Outline each blood parasite and name the species.
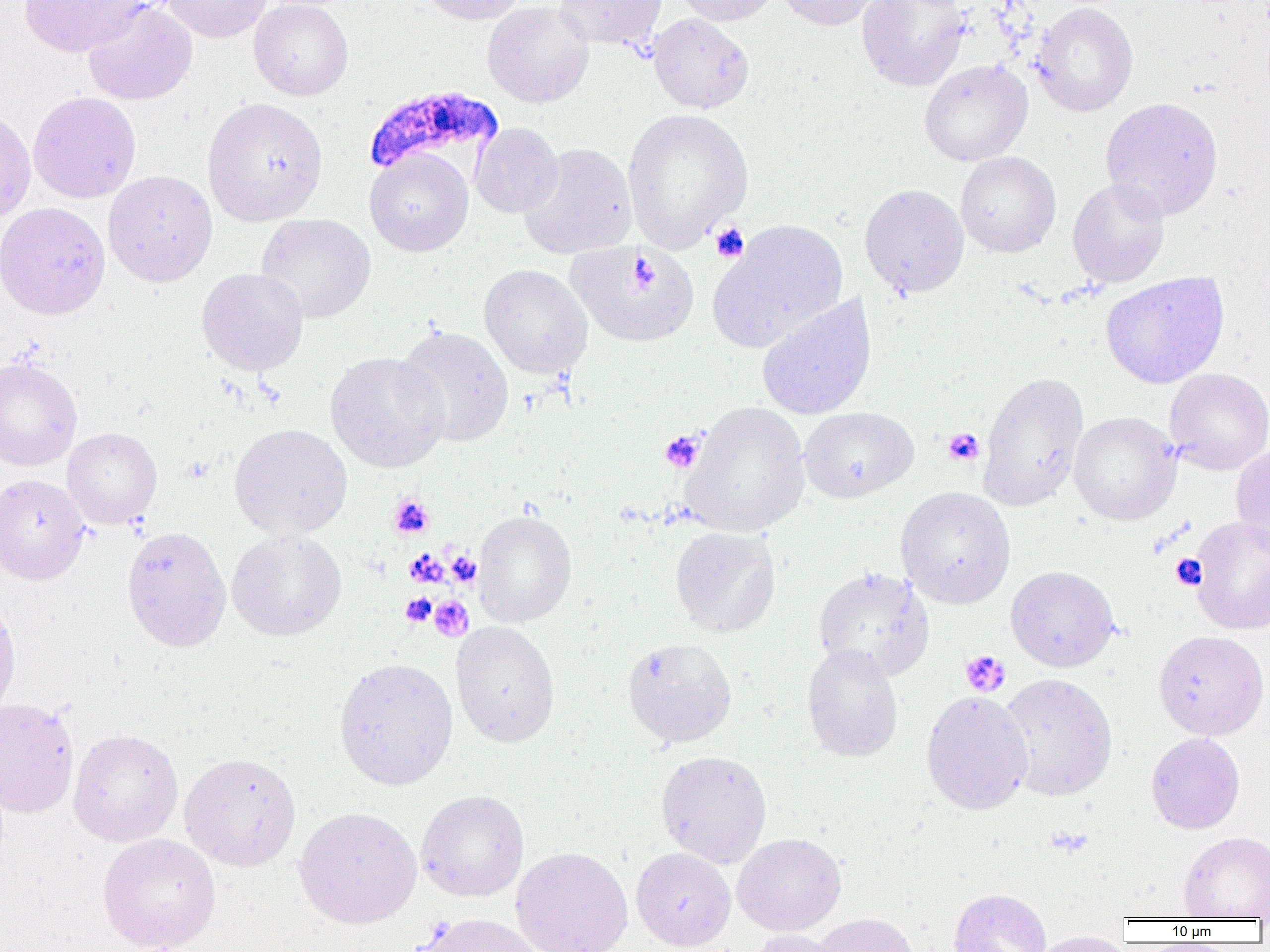
Approximate bounding boxes as (x1,y1)-(x2,y2) corner pairs in pixels.
Plasmodium falciparum-infected red blood cells: (362,86)-(504,181).
No Plasmodium ovale, Plasmodium malariae, Plasmodium vivax, Babesia divergens, or Trypanosoma brucei observed.

slide-level diagnosis = Plasmodium falciparum
field of view = single
preparation = thin blood film
modality = optical microscopy
magnification = 1000x
platelet locations = approximate bounding boxes as (x1,y1)-(x2,y2) corner pairs in pixels: (709,222)-(749,262), (943,428)-(984,466), (660,430)-(704,473), (388,493)-(435,539), (404,549)-(447,588), (447,550)-(481,586), (1172,555)-(1206,589), (400,593)-(436,627), (429,595)-(474,641), (960,650)-(1010,698)
image size = 1270×952 pixels
uninfected red blood cell locations = approximate bounding boxes as (x1,y1)-(x2,y2) corner pairs in pixels: (19,0)-(146,57), (162,0)-(272,43), (248,0)-(353,100), (419,0)-(524,25), (554,0)-(667,51), (675,0)-(780,26), (777,0)-(884,31), (857,0)-(970,91), (83,1)-(197,105), (482,1)-(594,108), (1031,2)-(1138,117), (648,13)-(754,113), (919,59)-(1032,166), (28,91)-(141,203), (1100,96)-(1223,221), (202,97)-(328,226), (0,108)-(36,222), (622,108)-(753,251), (470,122)-(563,218), (519,142)-(637,259), (364,148)-(474,257), (955,151)-(1061,258), (103,170)-(217,287), (1067,177)-(1170,288), (859,183)-(969,297), (0,202)-(111,319), (255,213)-(376,323), (710,220)-(847,352), (567,243)-(700,347), (479,264)-(593,379), (196,267)-(308,376), (1100,272)-(1230,389), (756,295)-(877,421), (394,324)-(515,447), (325,351)-(449,473), (0,356)-(82,470), (1164,368)-(1270,475), (978,371)-(1089,510), (680,401)-(810,537), (799,407)-(918,502), (1069,411)-(1181,525), (229,423)-(352,538), (62,427)-(162,529), (1231,444)-(1270,552), (0,474)-(89,584), (895,486)-(1016,609), (473,509)-(577,627), (1190,516)-(1270,635), (122,526)-(232,652), (670,526)-(781,638), (227,529)-(347,641), (812,565)-(935,681), (1005,565)-(1120,672), (0,592)-(21,720), (450,620)-(560,748), (1153,630)-(1269,739), (622,637)-(738,748), (801,643)-(903,763), (334,657)-(458,790), (999,673)-(1118,800), (920,690)-(1033,815), (0,697)-(79,818), (68,728)-(183,847), (1146,732)-(1245,834), (655,750)-(772,868), (179,752)-(301,871), (416,790)-(529,901), (294,806)-(422,928), (1178,832)-(1270,920), (97,833)-(221,952), (732,833)-(846,936), (511,846)-(633,952), (631,847)-(736,951), (949,888)-(1052,952), (415,913)-(544,952), (812,913)-(919,952), (748,929)-(846,952), (1028,931)-(1132,952)